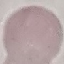 Malaria status: uninfected. Cell patch, automatically extracted from a larger field of view and resized to 64 × 64 pixels. Acquired by smartphone through the microscope eyepiece. Thin smear of blood. Giemsa stain.